State which parasite is depicted.
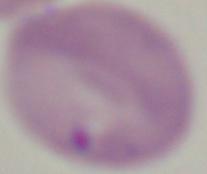

This is Babesia.

1000x magnification. Photomicrograph.